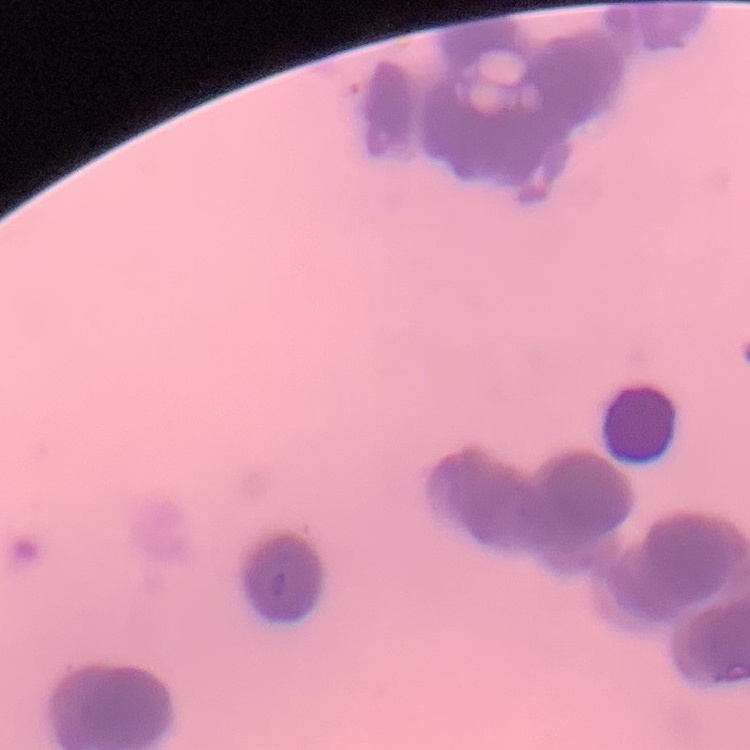 The erythrocytes exhibit rouleaux formation. Square crop of a larger photomicrograph. Stained with either Field's or Giemsa. Thin blood film.